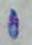
magnification = 1000x
modality = photomicrograph
identification = Toxoplasma gondii